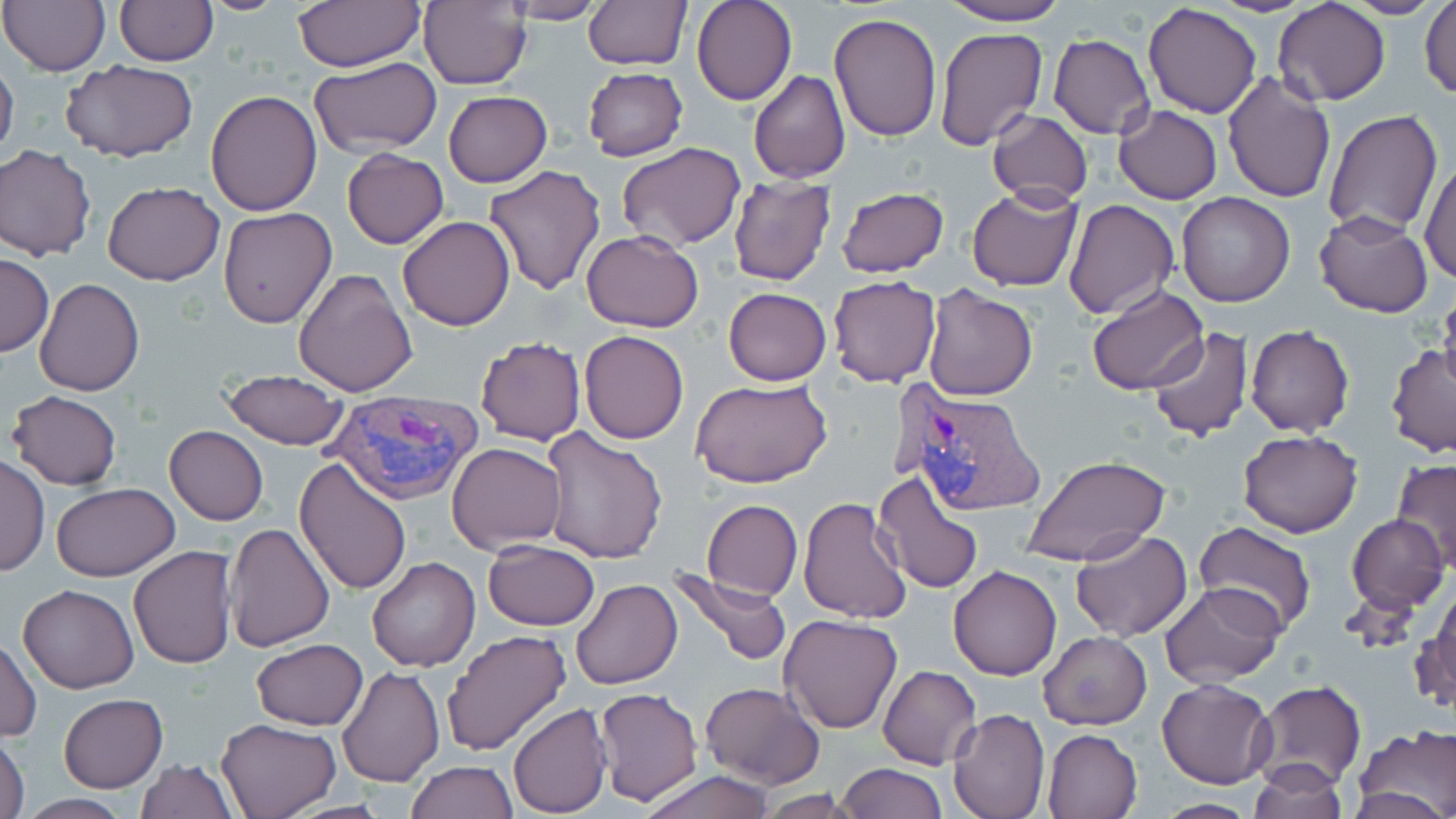
slide-level diagnosis = Plasmodium vivax
stain = May-Grünwald-Giemsa
field of view = single
image size = 1456×819 pixels
uninfected red blood cell locations = approximate bounding boxes as (x1, y1, x2, y2) in pixels: (0, 0, 111, 76), (198, 0, 293, 14), (418, 0, 533, 89), (583, 0, 689, 70), (692, 0, 796, 105), (935, 0, 1075, 25), (1205, 0, 1319, 16), (1343, 0, 1445, 19), (113, 1, 218, 66), (290, 1, 426, 71), (500, 1, 611, 24), (1419, 1, 1455, 101), (102, 2, 214, 138), (1273, 2, 1391, 106), (1143, 3, 1262, 118), (828, 13, 942, 141), (934, 28, 1047, 151), (1049, 34, 1155, 140), (1164, 39, 1301, 182), (0, 52, 19, 166), (309, 58, 442, 158), (61, 61, 200, 162), (582, 67, 689, 161), (749, 71, 850, 182), (1223, 72, 1336, 203), (205, 89, 323, 215), (443, 91, 552, 187), (1114, 104, 1222, 204), (986, 108, 1093, 206), (1324, 110, 1442, 238), (615, 142, 746, 251), (0, 144, 96, 261), (343, 148, 449, 248), (1420, 153, 1456, 287), (482, 165, 607, 296), (727, 173, 837, 285), (103, 182, 225, 285), (407, 186, 591, 314), (835, 186, 949, 277), (967, 186, 1082, 292), (1176, 193, 1295, 307), (1063, 198, 1178, 320), (219, 207, 337, 327), (1313, 211, 1433, 317), (397, 216, 516, 330), (581, 231, 703, 332), (0, 253, 52, 356), (294, 268, 418, 396), (828, 277, 940, 387), (34, 278, 144, 395), (863, 282, 990, 397), (921, 286, 1038, 401), (723, 287, 832, 386), (1086, 287, 1208, 396), (1439, 288, 1456, 398), (1245, 323, 1355, 438), (1146, 325, 1251, 444), (578, 331, 689, 444), (476, 337, 585, 446), (1385, 345, 1456, 456), (222, 369, 347, 450), (691, 377, 833, 490), (8, 391, 122, 490), (164, 426, 268, 525), (539, 427, 669, 563), (1238, 429, 1362, 538), (446, 442, 566, 554), (1, 454, 49, 577), (1025, 455, 1171, 571), (295, 459, 413, 595), (1393, 459, 1456, 571), (873, 469, 985, 596), (50, 482, 179, 582), (797, 496, 914, 623), (700, 500, 802, 601), (1347, 513, 1449, 613), (225, 523, 335, 651), (1192, 525, 1316, 637), (1069, 529, 1193, 643), (482, 539, 600, 631), (128, 545, 237, 668), (367, 557, 480, 672), (948, 566, 1063, 680), (672, 570, 790, 667), (570, 577, 683, 690), (1160, 582, 1285, 687), (1420, 582, 1455, 713), (18, 584, 140, 694), (779, 613, 903, 733), (440, 629, 569, 757), (1040, 632, 1152, 729), (1, 636, 41, 742), (251, 638, 368, 730), (877, 665, 981, 769), (338, 666, 444, 787), (1157, 679, 1276, 788), (1254, 680, 1365, 790), (699, 682, 825, 788), (594, 687, 703, 805), (58, 693, 167, 792), (508, 703, 611, 817), (947, 709, 1049, 819), (215, 718, 340, 818), (1353, 727, 1456, 813), (1042, 728, 1143, 819), (0, 732, 29, 819), (135, 758, 238, 818), (1245, 760, 1348, 817), (406, 761, 517, 818), (836, 763, 947, 819), (638, 770, 777, 819), (753, 791, 863, 818), (15, 795, 132, 817), (1152, 798, 1260, 817)
preparation = thin blood smear
Plasmodium vivax-infected red blood cell locations = approximate bounding boxes as (x1, y1, x2, y2) in pixels: (897, 387, 1047, 517), (326, 389, 485, 505)
modality = optical microscopy
magnification = 1000x